State the blood parasite species.
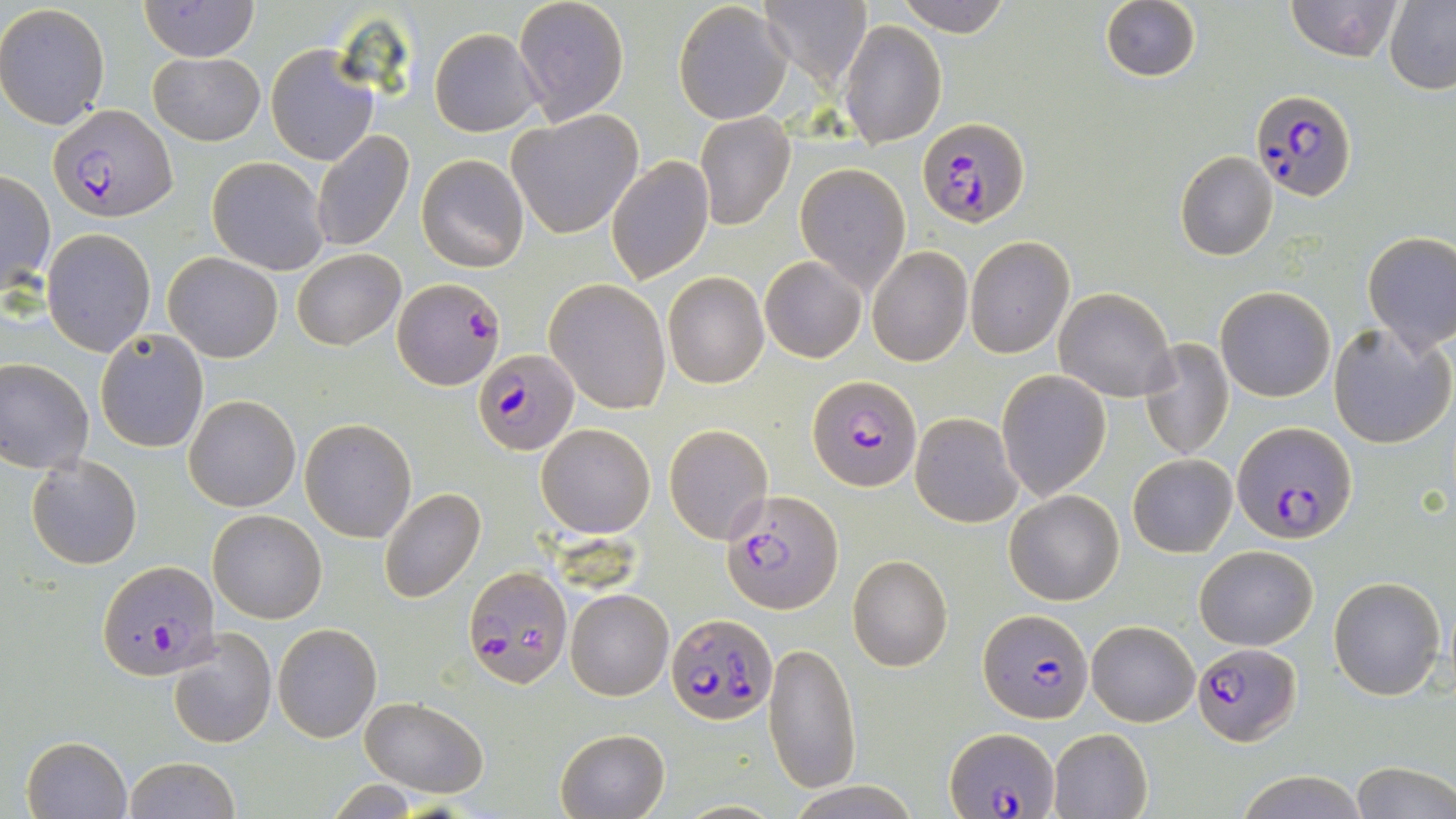
Plasmodium falciparum.

field_of_view: single
stain: May-Grünwald-Giemsa
preparation: thin blood smear
magnification: 1000x
uninfected_red_blood_cell_locations: 'approximate bounding boxes as (x1, y1, x2, y2) in pixels: (140, 0, 259, 61), (513, 0, 628, 125), (896, 0, 1011, 38), (1098, 0, 1201, 83), (1285, 0, 1405, 61), (759, 1, 873, 88), (674, 2, 791, 125), (1384, 2, 1456, 93), (0, 3, 110, 130), (840, 19, 946, 148), (429, 28, 542, 135), (266, 44, 379, 166), (148, 51, 265, 144), (505, 111, 643, 239), (695, 111, 795, 231), (310, 131, 414, 253), (1174, 151, 1279, 261), (416, 154, 529, 273), (606, 155, 715, 285), (207, 156, 329, 275), (795, 163, 910, 293), (1, 171, 54, 297), (42, 229, 155, 356), (1361, 231, 1456, 353), (965, 237, 1075, 357), (865, 246, 973, 367), (292, 249, 405, 350), (164, 251, 284, 363), (761, 256, 866, 362), (663, 272, 769, 389), (545, 279, 673, 414), (1215, 285, 1335, 402), (1054, 287, 1177, 402), (1328, 322, 1455, 450), (95, 329, 209, 451), (1138, 338, 1235, 461), (0, 358, 95, 473), (995, 368, 1111, 503), (185, 395, 300, 511), (911, 412, 1024, 528), (301, 418, 417, 542), (536, 423, 655, 537), (663, 423, 775, 546), (1128, 454, 1237, 557), (28, 455, 142, 570), (378, 488, 486, 604), (1005, 490, 1124, 605), (207, 509, 326, 624), (1195, 544, 1319, 650), (847, 555, 953, 672), (1329, 574, 1447, 701), (565, 588, 674, 700), (1087, 620, 1199, 727), (272, 622, 382, 742), (169, 628, 277, 748), (764, 641, 862, 794), (359, 696, 489, 796), (555, 727, 670, 818), (1047, 727, 1154, 819), (22, 735, 132, 819), (123, 756, 242, 819), (1350, 763, 1456, 819), (1231, 770, 1368, 818), (788, 780, 922, 818)'
modality: light microscopy
image_size: 1456×819 pixels
plasmodium_falciparum_infected_red_blood_cell_locations: 'approximate bounding boxes as (x1, y1, x2, y2) in pixels: (1250, 87, 1357, 201), (49, 103, 178, 223), (917, 117, 1030, 228), (391, 277, 504, 390), (473, 348, 579, 457), (809, 374, 920, 491), (1233, 421, 1357, 542), (723, 490, 845, 613), (96, 562, 221, 683), (464, 566, 574, 688), (978, 609, 1092, 725), (665, 614, 775, 725), (1193, 642, 1301, 747), (947, 726, 1056, 818)'